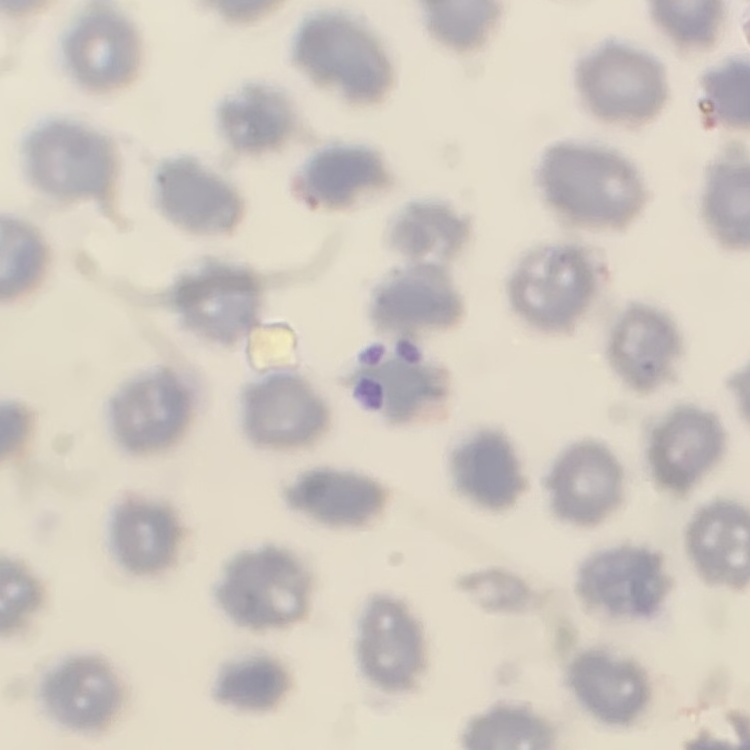

erythrocyte_morphology: no rouleaux formation
stain: Field's or Giemsa
preparation: thin peripheral smear
image_type: one tile cut from a larger photomicrograph